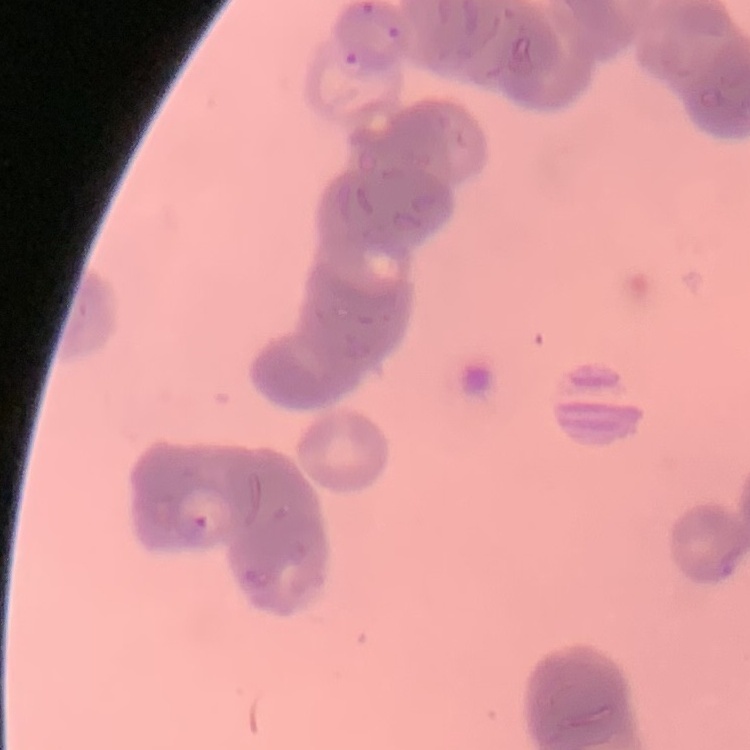 The erythrocytes show rouleaux formation. Stained with either Field's or Giemsa. One tile cut from a larger photomicrograph. Thin blood smear.